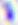 400x magnification. Micrograph. Toxoplasma gondii is shown.